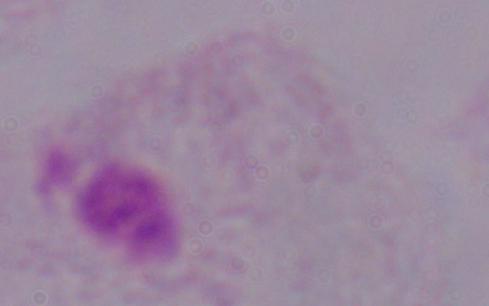

Photomicrograph. A trichomonad is shown. Captured at 1000x magnification.